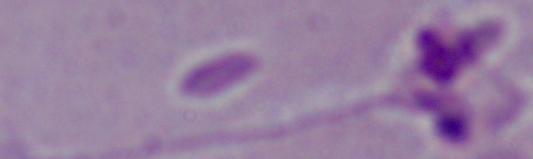 Micrograph. 1000x magnification. A Leishmania parasite is shown.